Classify this cell by malaria status.
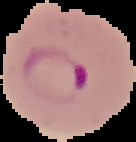
Parasitized.

image type = segmented cell region on a black background
image size = 136×142 pixels
preparation = thin blood smear